Name the parasite shown.
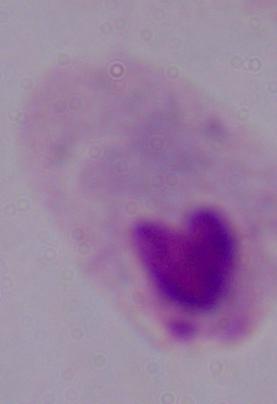

This is a trichomonad.

Summary:
  - Magnification: 1000x
  - Modality: photomicrograph